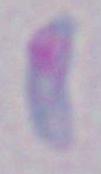

Micrograph. 1000x magnification. Toxoplasma gondii is shown.